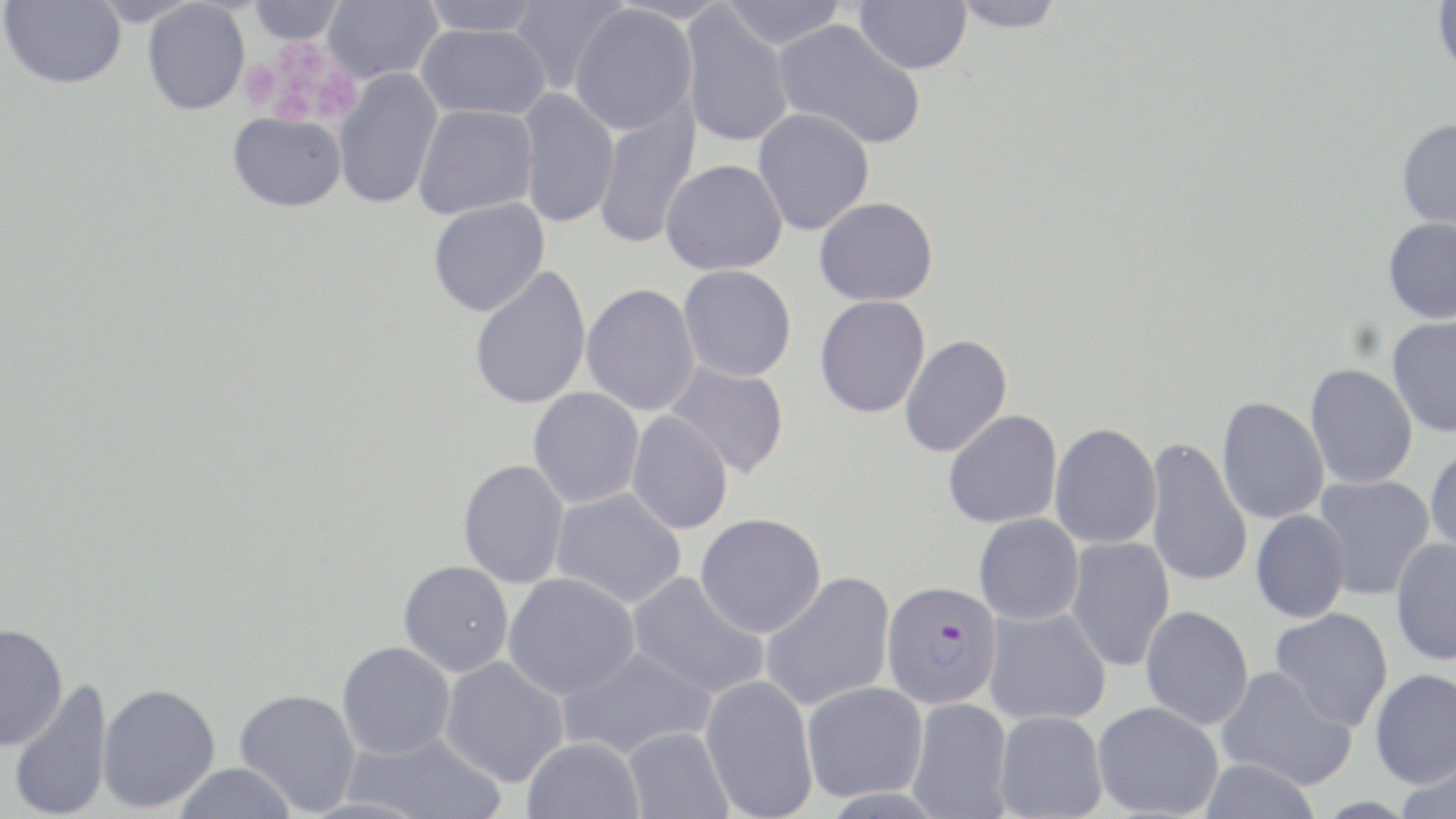

slide-level diagnosis = Plasmodium falciparum
stain = May-Grünwald-Giemsa
preparation = thin blood smear
image size = 1456×819 pixels
modality = optical microscopy
magnification = 1000x
platelet locations = approximate bounding boxes as named x1/y1/x2/y2 corners in pixels: (x1=272, y1=41, x2=330, y2=90), (x1=240, y1=60, x2=280, y2=110), (x1=315, y1=72, x2=358, y2=123), (x1=272, y1=87, x2=320, y2=127)
uninfected red blood cell locations = approximate bounding boxes as named x1/y1/x2/y2 corners in pixels: (x1=1, y1=0, x2=126, y2=89), (x1=248, y1=0, x2=344, y2=44), (x1=323, y1=0, x2=443, y2=83), (x1=421, y1=0, x2=546, y2=36), (x1=509, y1=0, x2=628, y2=95), (x1=719, y1=0, x2=848, y2=49), (x1=855, y1=0, x2=971, y2=74), (x1=946, y1=0, x2=1068, y2=33), (x1=1432, y1=0, x2=1456, y2=80), (x1=142, y1=1, x2=250, y2=115), (x1=568, y1=5, x2=697, y2=135), (x1=680, y1=9, x2=793, y2=148), (x1=773, y1=19, x2=926, y2=150), (x1=416, y1=23, x2=551, y2=120), (x1=333, y1=69, x2=443, y2=210), (x1=516, y1=88, x2=620, y2=229), (x1=594, y1=101, x2=701, y2=250), (x1=413, y1=104, x2=538, y2=220), (x1=753, y1=107, x2=874, y2=235), (x1=227, y1=112, x2=346, y2=212), (x1=1396, y1=118, x2=1456, y2=234), (x1=660, y1=159, x2=788, y2=275), (x1=814, y1=196, x2=939, y2=306), (x1=427, y1=198, x2=550, y2=317), (x1=1383, y1=217, x2=1456, y2=323), (x1=678, y1=265, x2=797, y2=381), (x1=469, y1=266, x2=592, y2=410), (x1=581, y1=283, x2=701, y2=416), (x1=815, y1=295, x2=931, y2=418), (x1=1387, y1=316, x2=1456, y2=438), (x1=899, y1=335, x2=1012, y2=458), (x1=664, y1=361, x2=790, y2=479), (x1=1305, y1=363, x2=1418, y2=489), (x1=528, y1=387, x2=645, y2=508), (x1=1216, y1=396, x2=1329, y2=524), (x1=943, y1=410, x2=1062, y2=529), (x1=626, y1=411, x2=734, y2=535), (x1=1049, y1=423, x2=1162, y2=549), (x1=1144, y1=437, x2=1253, y2=590), (x1=1425, y1=444, x2=1456, y2=559), (x1=458, y1=460, x2=570, y2=588), (x1=1313, y1=475, x2=1435, y2=600), (x1=551, y1=487, x2=686, y2=609), (x1=1250, y1=510, x2=1351, y2=623), (x1=695, y1=513, x2=826, y2=637), (x1=974, y1=513, x2=1084, y2=625), (x1=1065, y1=537, x2=1175, y2=672), (x1=1390, y1=538, x2=1456, y2=665), (x1=398, y1=560, x2=514, y2=677), (x1=759, y1=571, x2=896, y2=712), (x1=503, y1=572, x2=640, y2=699), (x1=627, y1=572, x2=768, y2=699), (x1=1140, y1=606, x2=1255, y2=730), (x1=984, y1=607, x2=1111, y2=726), (x1=1270, y1=607, x2=1394, y2=732), (x1=0, y1=624, x2=67, y2=751), (x1=337, y1=642, x2=455, y2=759), (x1=558, y1=646, x2=717, y2=760), (x1=439, y1=656, x2=569, y2=787), (x1=1216, y1=666, x2=1356, y2=790), (x1=1369, y1=669, x2=1456, y2=789), (x1=700, y1=674, x2=818, y2=818), (x1=8, y1=678, x2=113, y2=819), (x1=801, y1=681, x2=928, y2=802), (x1=96, y1=683, x2=220, y2=813), (x1=234, y1=688, x2=361, y2=815), (x1=907, y1=697, x2=1013, y2=819), (x1=1092, y1=701, x2=1224, y2=818), (x1=994, y1=710, x2=1108, y2=819), (x1=622, y1=727, x2=733, y2=819), (x1=344, y1=730, x2=506, y2=819), (x1=522, y1=737, x2=645, y2=819), (x1=1396, y1=753, x2=1456, y2=819), (x1=1199, y1=757, x2=1321, y2=819), (x1=173, y1=763, x2=297, y2=819)
field of view = single
Plasmodium falciparum-infected red blood cell locations = approximate bounding boxes as named x1/y1/x2/y2 corners in pixels: (x1=881, y1=580, x2=1001, y2=708)